Assess this cell for malaria.
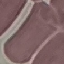

Uninfected.

Automatically extracted cell patch, resized to 64 × 64 pixels. Thin smear of blood. Photographed with a smartphone camera at the microscope eyepiece. Giemsa stain.